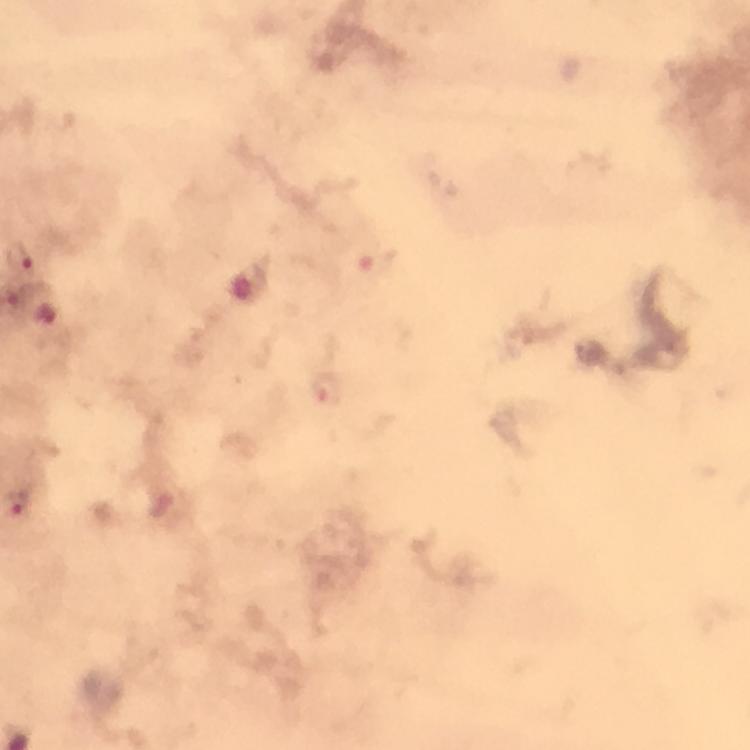 Approximate centers as {x, y} in pixels. Malaria parasite locations: {18, 258}, {374, 264}, {49, 315}, {326, 389}. Cropped region of a single field of view. Image is 750×750 pixels. At 100x magnification. Immersion oil was used. From a malaria diagnostic workup. Giemsa stain. Thick smear. Photographed through the microscope with a smartphone camera.